Assess this cell for malaria.
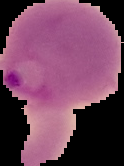

Parasitized.

image type = segmented cell region with the area outside set to black
preparation = thin blood film
image size = 124×166 pixels